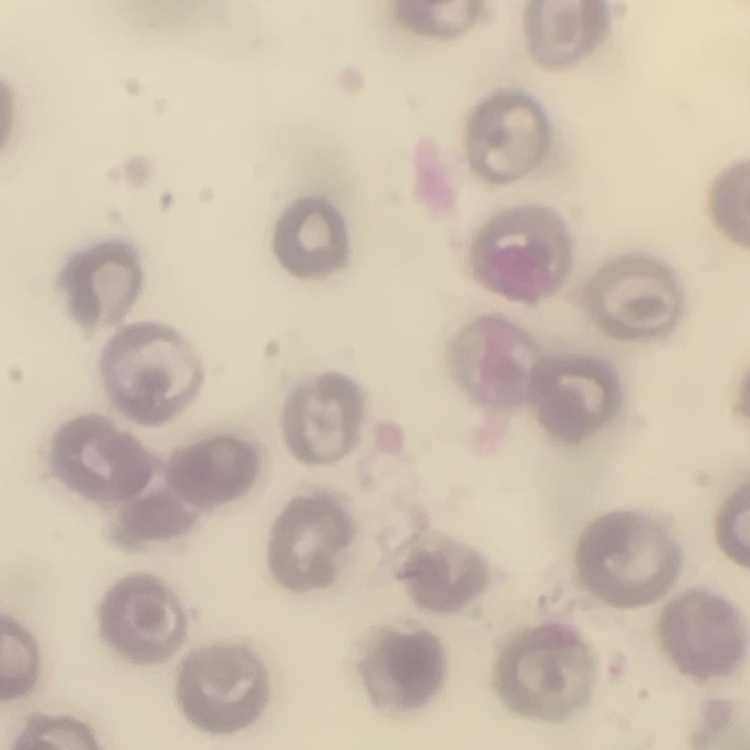

The erythrocytes show no rouleaux formation. Stained with either Field's or Giemsa. Thin peripheral smear. One tile cut from a larger photomicrograph.